Locate every blood parasite and identify its species.
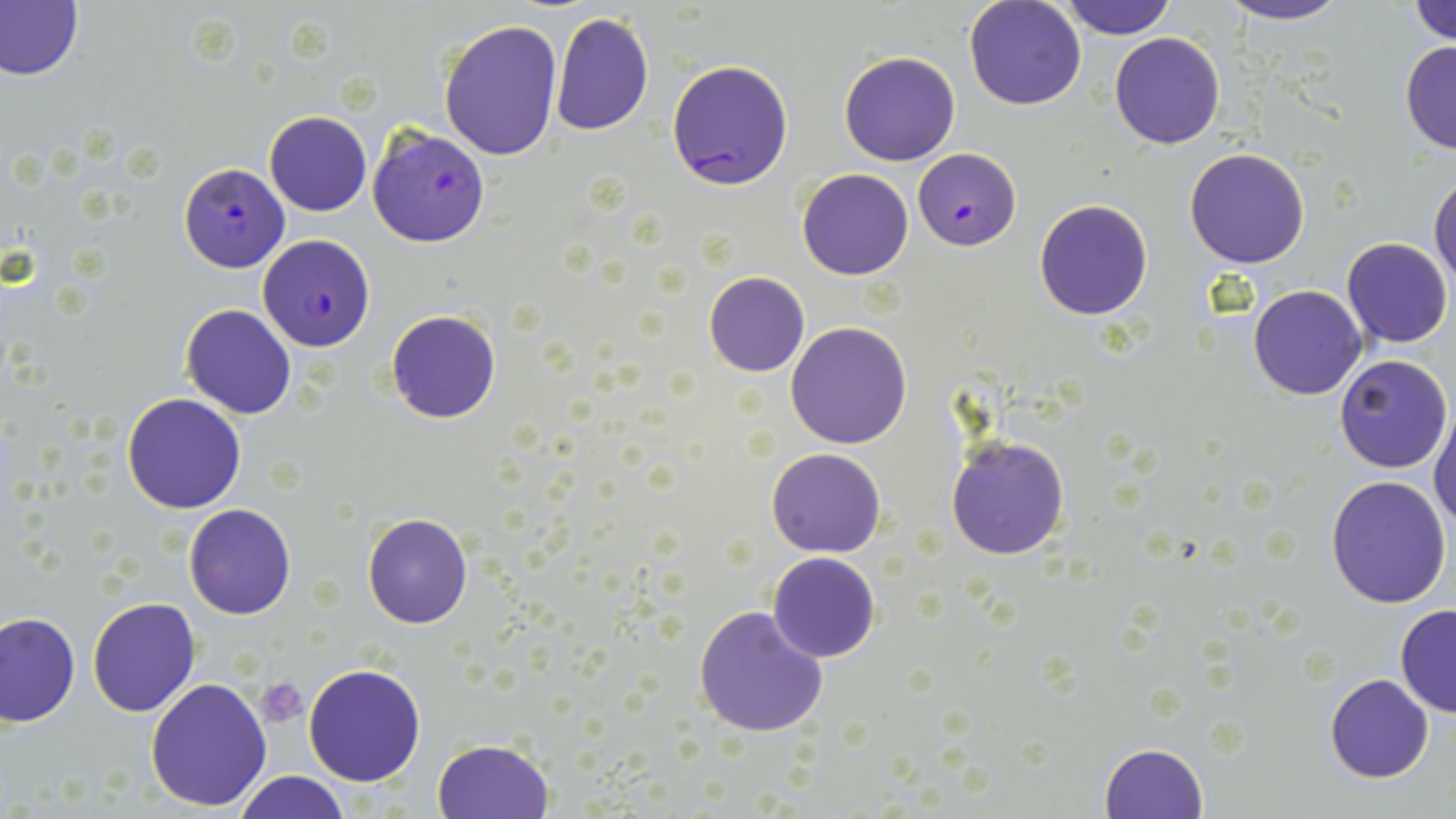

Approximate bounding boxes as [x1, y1, x2, y2] in pixels.
Plasmodium falciparum-infected red blood cells: [666, 58, 794, 191], [368, 126, 490, 247], [914, 149, 1018, 252], [179, 163, 289, 272], [257, 234, 375, 351].
No Plasmodium ovale, Plasmodium malariae, Plasmodium vivax, Babesia divergens, or Trypanosoma brucei observed.

Uninfected red blood cell locations: [964, 0, 1087, 110], [1058, 0, 1180, 40], [1216, 0, 1353, 26], [1409, 0, 1456, 47], [0, 1, 84, 82], [549, 9, 654, 137], [438, 20, 563, 161], [1110, 32, 1225, 149], [1399, 39, 1456, 155], [837, 50, 961, 166], [264, 110, 372, 216], [1184, 148, 1310, 268], [795, 169, 914, 280], [1430, 173, 1456, 294], [1033, 198, 1154, 321], [1342, 237, 1453, 348], [703, 271, 811, 377], [1247, 283, 1368, 400], [180, 304, 298, 419], [386, 310, 501, 423], [785, 321, 912, 449], [1335, 355, 1453, 474], [122, 392, 247, 513], [1430, 404, 1456, 534], [945, 434, 1069, 561], [766, 447, 887, 558], [1326, 477, 1451, 609], [184, 503, 296, 619], [362, 511, 473, 629], [767, 552, 880, 662], [87, 597, 199, 718], [692, 603, 830, 739], [1395, 603, 1455, 718], [0, 611, 79, 727], [303, 663, 426, 786], [1324, 674, 1433, 783], [145, 676, 275, 813], [432, 739, 554, 819], [1099, 742, 1209, 817], [234, 771, 350, 819]. Platelet locations: [257, 676, 309, 727]. Slide-level diagnosis: Plasmodium falciparum. Image is 1456×819 pixels. Captured at 1000x magnification. Optical microscopy. Thin blood film. May-Grünwald-Giemsa stain. Single field of view.